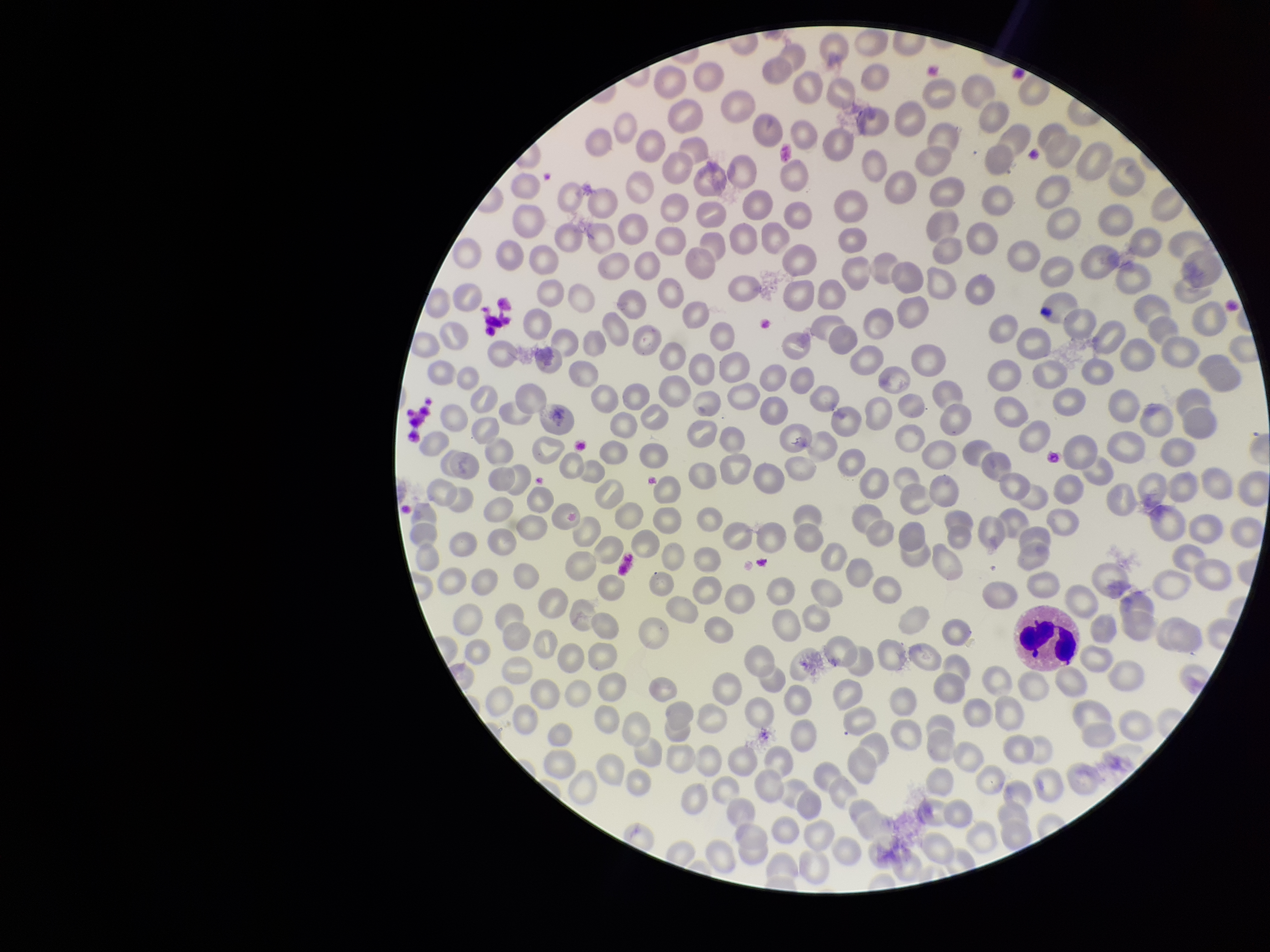

Summary:
  - Image size: 1270×952 pixels
  - Red blood cell count: 243
  - Preparation: thin smear
  - Parasitized red blood cell count: 0
  - Patient malaria status: negative
  - Capture: smartphone photograph through the microscope eyepiece
  - Parasitized red blood cells: none seen
  - Stain: Giemsa
  - Field of view: one from this slide